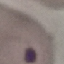
{
  "result": "malaria parasites identified",
  "stain": "Giemsa",
  "preparation": "thin smear",
  "capture": "smartphone through the microscope eyepiece",
  "image_type": "cell patch, automatically extracted from a larger field of view and resized to 64 × 64 pixels"
}